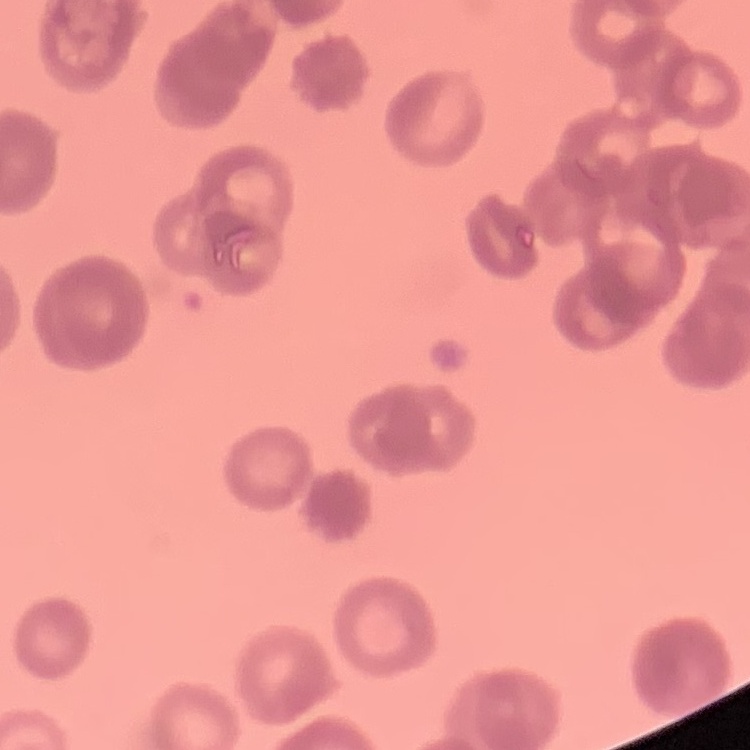 The erythrocytes exhibit rouleaux formation. Thin peripheral smear. One tile cut from a larger photomicrograph. Field's or Giemsa stain.